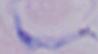

A trypanosome is seen. Micrograph. 1000x magnification.